Identify the parasite.
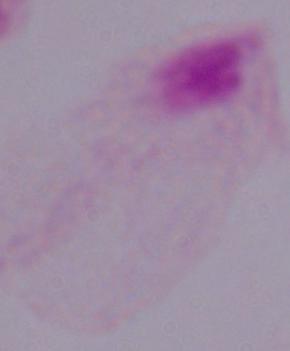

This is a trichomonad.

Micrograph. 1000x magnification.